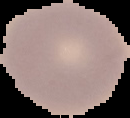

Summary:
  - Result: no malaria parasites seen
  - Image size: 130×118 pixels
  - Preparation: thin blood smear
  - Image type: segmented cell region on a black background